State which cell type is depicted.
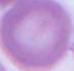
An erythrocyte.

Photomicrograph. 1000x magnification.